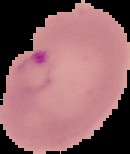
image size = 130×154 pixels
preparation = thin blood film
malaria status = parasitized
image type = cell region segmented out of the field of view; surrounding area masked to black